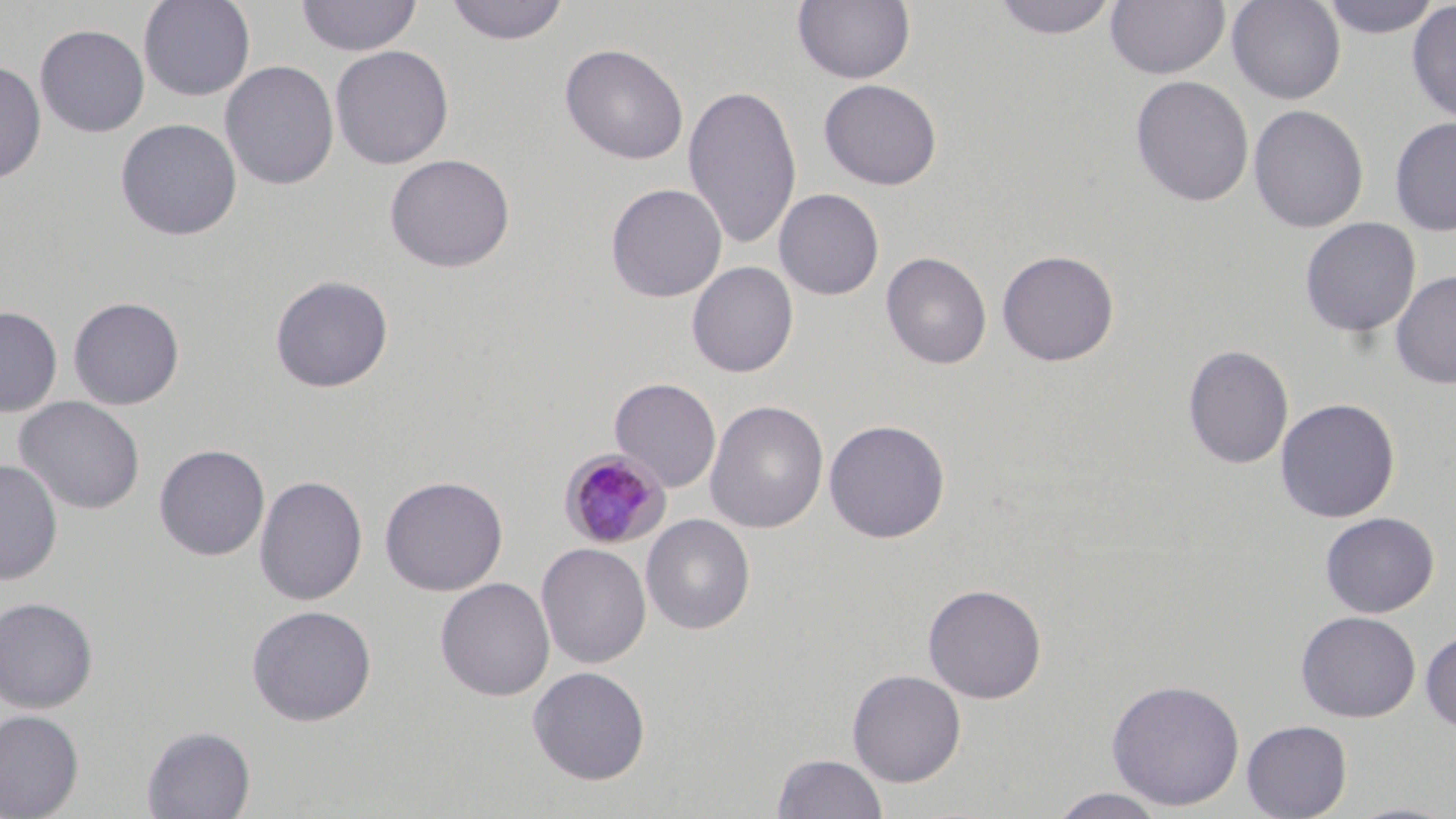

Approximate bounding boxes as [x1, y1, x2, y2] in pixels. Uninfected red blood cell locations: [138, 0, 256, 102], [295, 0, 422, 57], [443, 0, 570, 45], [792, 0, 915, 85], [989, 0, 1120, 40], [1105, 0, 1230, 80], [1226, 0, 1346, 105], [1318, 0, 1443, 39], [1406, 2, 1456, 123], [34, 24, 150, 138], [559, 43, 689, 165], [329, 44, 454, 169], [0, 60, 46, 184], [219, 60, 339, 191], [1130, 75, 1254, 207], [818, 79, 942, 190], [683, 83, 802, 251], [1247, 104, 1368, 234], [1389, 116, 1456, 235], [115, 118, 242, 241], [384, 153, 516, 273], [605, 183, 727, 303], [774, 188, 884, 301], [1299, 217, 1421, 338], [996, 248, 1120, 367], [880, 252, 992, 370], [686, 262, 798, 378], [1390, 270, 1456, 390], [269, 275, 394, 393], [67, 296, 185, 410], [0, 305, 62, 417], [1182, 344, 1294, 470], [609, 378, 722, 492], [13, 396, 146, 515], [1275, 397, 1400, 523], [704, 400, 829, 534], [823, 419, 950, 543], [154, 444, 270, 561], [0, 459, 63, 586], [254, 474, 368, 607], [379, 475, 508, 596], [1320, 512, 1439, 618], [641, 514, 755, 634], [536, 542, 651, 669], [434, 577, 555, 701], [922, 583, 1047, 704], [0, 596, 99, 713], [246, 604, 377, 726], [1296, 610, 1421, 723], [1420, 630, 1456, 732], [527, 665, 651, 785], [847, 669, 966, 786], [1105, 678, 1246, 810], [0, 709, 84, 819], [1241, 719, 1352, 819], [141, 725, 257, 818], [773, 752, 887, 819], [1047, 788, 1169, 818], [1340, 801, 1456, 819]. Plasmodium malariae-infected red blood cell locations: [558, 448, 671, 550]. Slide-level diagnosis: Plasmodium malariae. Thin blood smear. Image is 1456×819 pixels. Captured at 1000x magnification. May-Grünwald-Giemsa stain. Light microscopy. Single field of view.